Describe the morphology of the red blood cells.
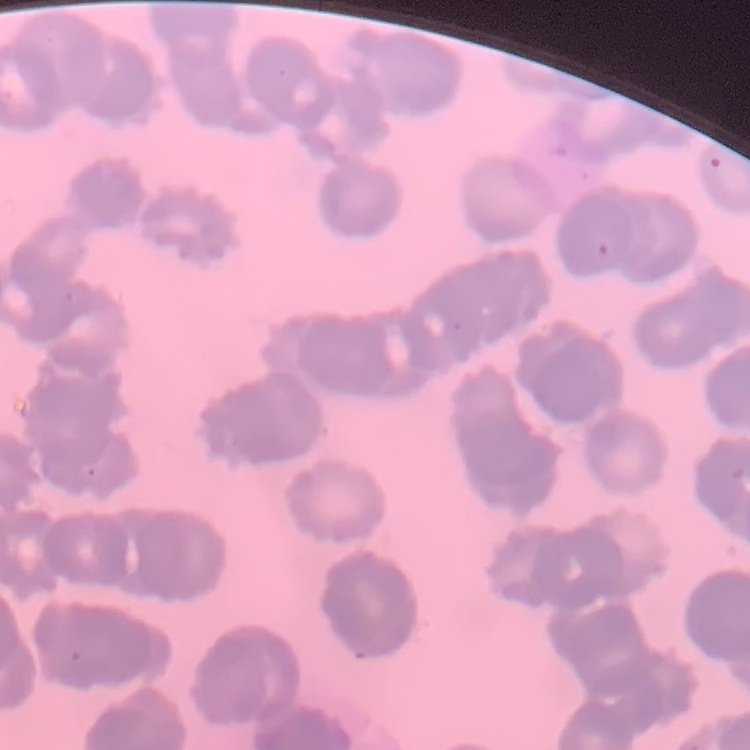

They show rouleaux formation.

image_type: square crop of a larger photomicrograph
preparation: thin blood smear
stain: Field's or Giemsa